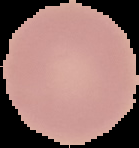

image size = 139×148 pixels
preparation = thin blood film
image type = cell region segmented out of the field of view; surrounding area masked to black
malaria status = uninfected